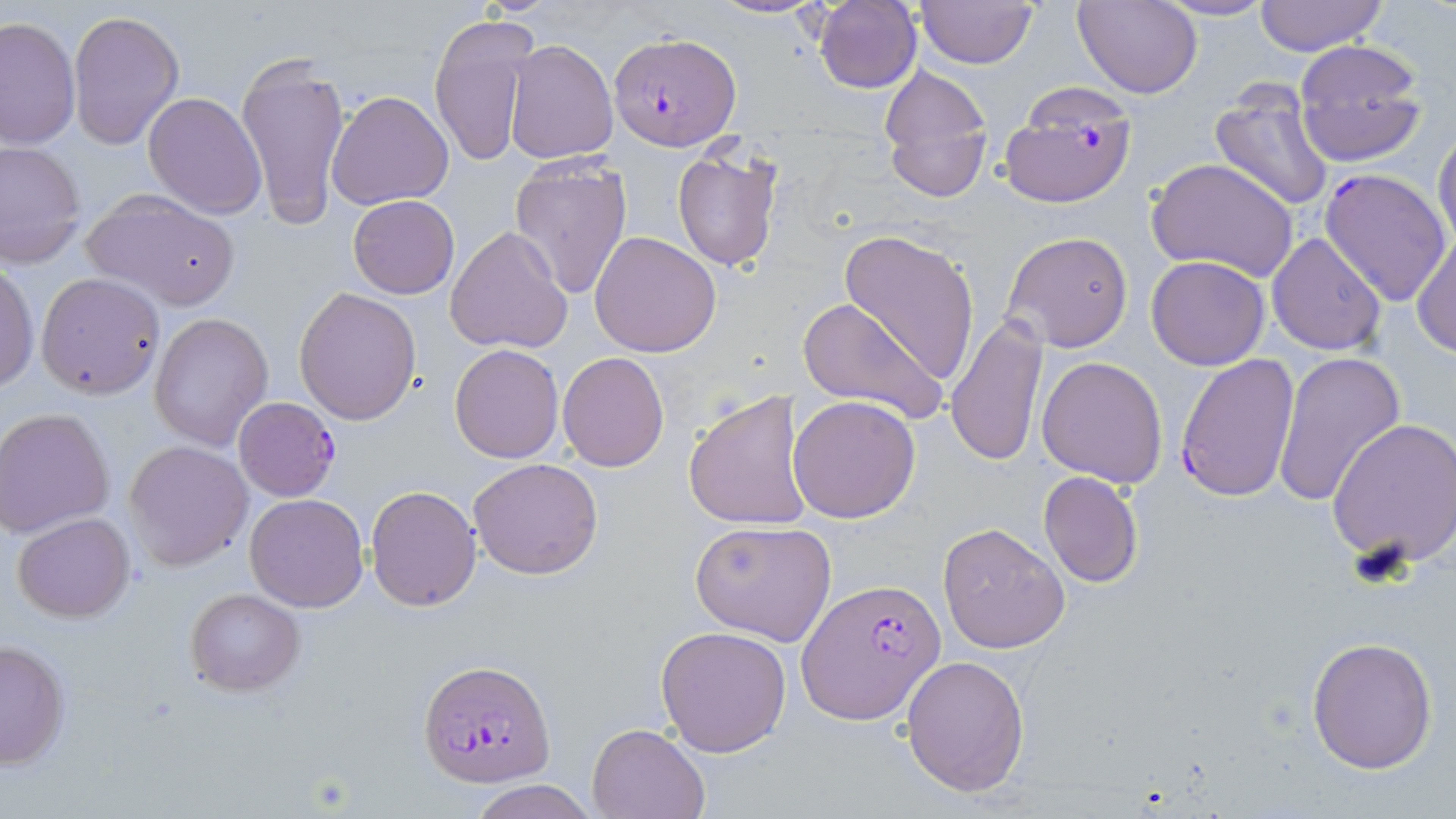

{
  "slide_level_diagnosis": "Plasmodium falciparum",
  "image_size": "1456×819 pixels",
  "plasmodium_falciparum_infected_red_blood_cell_locations": "approximate bounding boxes as (x1, y1, x2, y2) in pixels: (611, 30, 742, 152), (1000, 85, 1138, 208), (1319, 166, 1452, 308), (1175, 351, 1301, 504), (233, 396, 342, 502), (798, 577, 946, 724), (420, 659, 556, 786)",
  "modality": "optical microscopy",
  "uninfected_red_blood_cell_locations": "approximate bounding boxes as (x1, y1, x2, y2) in pixels: (708, 0, 826, 19), (812, 0, 923, 93), (1153, 0, 1279, 22), (1254, 0, 1386, 55), (917, 1, 1038, 68), (1073, 1, 1204, 99), (68, 10, 184, 150), (427, 13, 537, 171), (0, 16, 80, 152), (503, 39, 618, 165), (1292, 41, 1425, 165), (236, 54, 352, 228), (876, 66, 994, 202), (1210, 82, 1336, 212), (327, 90, 454, 210), (143, 92, 267, 219), (1433, 125, 1456, 251), (1, 140, 87, 267), (673, 147, 783, 272), (507, 156, 634, 300), (1148, 158, 1299, 282), (83, 190, 240, 310), (348, 195, 459, 299), (445, 225, 574, 355), (835, 228, 982, 385), (1413, 229, 1455, 359), (590, 231, 722, 358), (1002, 231, 1134, 352), (1266, 231, 1385, 356), (1146, 256, 1270, 370), (0, 262, 38, 393), (36, 272, 166, 399), (294, 286, 422, 424), (797, 296, 946, 424), (148, 313, 273, 451), (946, 319, 1049, 467), (448, 344, 563, 464), (557, 352, 671, 473), (1274, 353, 1406, 507), (1037, 355, 1168, 488), (683, 389, 813, 532), (789, 395, 920, 522), (1, 408, 116, 539), (1328, 417, 1456, 569), (124, 440, 254, 570), (468, 457, 604, 579), (1037, 471, 1144, 588), (366, 485, 481, 612), (244, 494, 368, 611), (11, 512, 134, 623), (689, 519, 837, 645), (938, 523, 1070, 654), (184, 588, 304, 695), (655, 625, 792, 757), (1306, 636, 1438, 774), (0, 638, 70, 770), (902, 654, 1031, 797), (586, 721, 711, 818), (470, 780, 596, 819)",
  "field_of_view": "one of a larger specimen",
  "stain": "May-Grünwald-Giemsa",
  "preparation": "thin blood film",
  "magnification": "1000x"
}